Find each parasitized red blood cell.
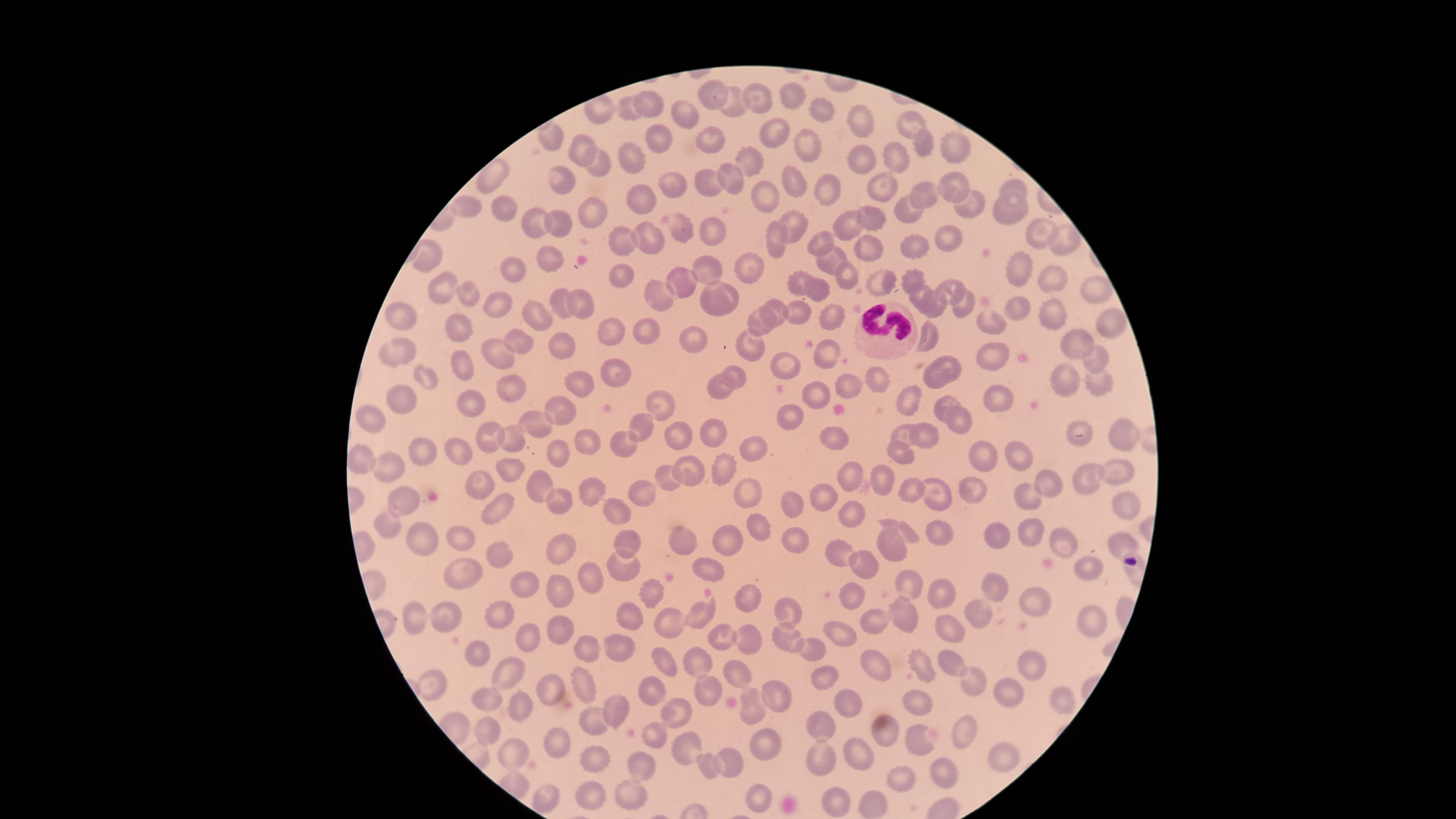
No parasitized red blood cells identified.

preparation = thin smear of blood
field of view = single
stain = Giemsa
image size = 1456×819 pixels
white blood cells = approximate marker points as [x, y] in pixels: [881, 328]
capture = smartphone photograph through the microscope eyepiece
uninfected red blood cells = approximate marker points as [x, y] in pixels: [794, 97], [753, 98], [711, 100], [653, 105], [731, 107], [821, 109], [630, 111], [686, 112], [908, 119], [856, 124], [774, 135], [552, 138], [660, 139], [714, 143], [927, 144], [580, 145], [959, 148], [807, 149], [633, 154], [897, 155], [598, 163], [752, 165], [861, 165], [491, 175], [672, 181], [731, 181], [560, 182], [708, 184], [953, 185], [800, 186], [884, 186], [827, 189], [1011, 191], [766, 192], [926, 193], [646, 199], [969, 204], [463, 205], [910, 207], [497, 208], [582, 213], [1006, 213], [870, 219], [798, 220], [536, 226], [845, 226], [563, 228], [682, 232], [1038, 234], [712, 235], [777, 237], [647, 238], [1067, 240], [816, 241], [951, 241], [626, 242], [868, 244], [915, 245], [422, 253], [823, 258], [546, 259], [751, 260], [714, 265], [1016, 266], [624, 267], [512, 272], [843, 275], [684, 276], [1048, 279], [886, 280], [797, 281], [913, 282], [1093, 286], [441, 287], [952, 287], [820, 292], [661, 293], [922, 294], [470, 297], [718, 297], [563, 301], [580, 303], [937, 304], [965, 305], [497, 309], [776, 310], [1021, 312], [798, 313], [823, 314], [539, 316], [1050, 317], [406, 321], [986, 321], [461, 323], [764, 324], [1106, 324], [646, 330], [612, 335], [929, 337], [562, 339], [697, 339], [521, 340], [1078, 342], [755, 346], [397, 351], [823, 354], [1093, 355], [503, 356], [990, 356], [791, 365], [954, 365], [466, 366], [732, 373], [424, 374], [621, 376], [875, 378], [931, 378], [1068, 378], [1097, 378], [583, 379], [722, 382], [848, 386], [520, 388], [405, 394], [817, 395], [994, 397], [906, 400], [476, 405], [655, 405], [945, 405], [567, 409], [377, 416], [787, 417], [956, 419], [533, 423], [1075, 425], [642, 431], [905, 432], [1123, 432], [488, 433], [516, 433], [713, 434], [925, 436], [683, 437], [592, 439], [836, 439], [626, 441], [754, 445], [901, 447], [555, 448], [455, 451], [982, 451], [421, 454], [1020, 455], [362, 456], [391, 462], [1117, 470], [514, 471], [692, 471], [721, 472], [846, 473], [1086, 477], [671, 478], [880, 478], [1050, 482], [479, 483], [537, 483], [592, 485], [643, 490], [907, 490], [750, 491], [974, 492], [935, 494], [1025, 496], [826, 497], [399, 499], [788, 499], [563, 500], [1123, 506], [615, 509], [500, 511], [853, 515], [754, 525], [390, 526], [1033, 531], [908, 532], [457, 533], [939, 533], [998, 536], [420, 539], [725, 539], [1062, 539], [797, 541], [631, 543], [680, 543], [1121, 544], [892, 546], [499, 552], [559, 553], [842, 554], [861, 558], [708, 569], [1086, 569], [625, 570], [466, 571], [587, 577], [911, 582], [527, 587], [994, 588], [851, 590], [650, 591], [557, 592], [750, 596], [940, 596], [1035, 602], [504, 606], [790, 609], [900, 610], [411, 611], [631, 615], [699, 615], [448, 617], [973, 617], [1093, 619], [869, 625], [559, 626], [668, 626], [947, 627], [783, 631], [725, 637], [749, 639], [842, 640], [528, 646], [588, 646], [480, 650], [617, 650], [812, 651], [948, 660], [704, 664], [666, 665], [867, 667], [1031, 667], [512, 668], [922, 669], [739, 676], [823, 680], [976, 682], [588, 686], [1006, 688], [433, 690], [649, 690], [549, 692], [705, 693], [775, 694], [919, 698], [1065, 698], [490, 700], [847, 703], [614, 705], [751, 708], [518, 709], [675, 709], [594, 722], [823, 724], [490, 729], [969, 731], [654, 734], [887, 734], [765, 740], [923, 741], [554, 745], [691, 750], [512, 751], [597, 754], [1001, 756], [864, 757], [731, 759], [824, 761], [709, 762], [646, 767], [948, 772], [905, 780], [588, 788], [626, 795], [547, 796], [761, 798], [833, 800], [873, 803]
visible region = circular